State which parasite is depicted.
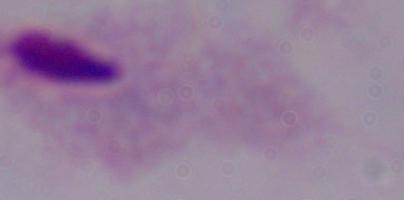

This is a trichomonad.

Summary:
  - Magnification: 1000x
  - Modality: micrograph